Report the malaria status of this cell.
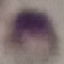

It is uninfected.

Summary:
  - Stain: Giemsa
  - Capture: smartphone camera at the microscope eyepiece
  - Image type: cell patch, automatically extracted from a larger field of view and resized to 64 × 64 pixels
  - Preparation: thin smear